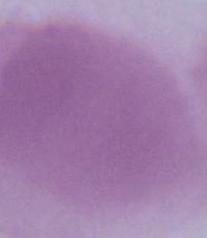
Summary:
  - Identification: erythrocyte
  - Modality: photomicrograph
  - Magnification: 1000x